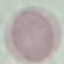

Summary:
  - Malaria status: uninfected
  - Capture: smartphone camera at the microscope eyepiece
  - Preparation: thin blood smear
  - Stain: Giemsa
  - Image type: cell patch, automatically extracted from a larger field of view and resized to 64 × 64 pixels